Locate every blood parasite and identify its species.
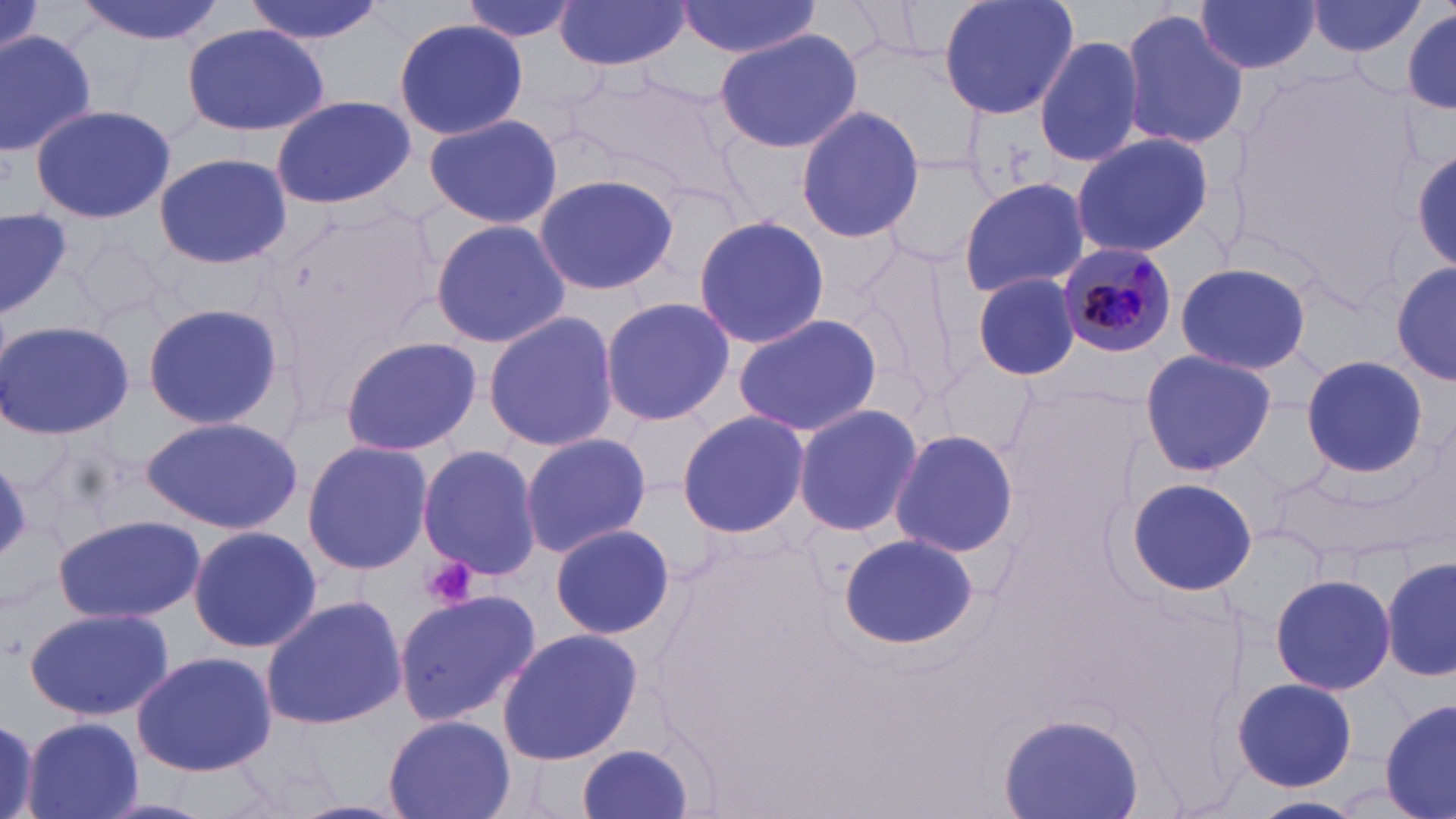
Approximate bounding boxes as (x1, y1, x2, y2) in pixels.
Plasmodium malariae-infected red blood cells: (1057, 242, 1182, 359).
No Plasmodium falciparum, Plasmodium ovale, Plasmodium vivax, Babesia divergens, or Trypanosoma brucei observed.

slide-level diagnosis = Plasmodium malariae
uninfected red blood cell locations = approximate bounding boxes as (x1, y1, x2, y2) in pixels: (70, 0, 230, 44), (243, 0, 382, 45), (465, 0, 578, 45), (939, 0, 1080, 123), (1194, 0, 1321, 75), (675, 1, 820, 58), (1306, 1, 1427, 58), (554, 2, 691, 70), (1398, 5, 1455, 117), (1121, 8, 1246, 152), (394, 16, 527, 140), (179, 23, 331, 137), (714, 28, 863, 155), (0, 29, 99, 157), (1035, 34, 1143, 170), (560, 70, 740, 191), (270, 95, 414, 209), (29, 102, 176, 226), (795, 103, 925, 246), (422, 112, 563, 231), (1068, 131, 1215, 259), (1409, 139, 1456, 279), (874, 147, 996, 267), (153, 152, 291, 270), (532, 170, 679, 298), (957, 178, 1091, 299), (261, 193, 445, 362), (0, 208, 72, 317), (693, 213, 830, 350), (429, 218, 570, 350), (67, 228, 171, 334), (846, 234, 971, 408), (1173, 260, 1314, 376), (1392, 262, 1453, 389), (970, 271, 1083, 381), (598, 296, 734, 428), (141, 301, 284, 431), (484, 311, 620, 452), (733, 312, 884, 437), (0, 318, 134, 442), (337, 336, 479, 456), (1139, 350, 1276, 477), (1301, 355, 1428, 477), (791, 402, 922, 538), (677, 407, 812, 540), (140, 414, 303, 533), (889, 426, 1020, 559), (519, 432, 653, 558), (301, 440, 435, 576), (417, 445, 544, 580), (1123, 476, 1258, 597), (55, 514, 201, 624), (550, 523, 675, 641), (184, 526, 324, 654), (835, 532, 982, 650), (1382, 556, 1456, 683), (1269, 571, 1396, 695), (397, 590, 541, 726), (259, 595, 409, 730), (25, 606, 174, 721), (496, 628, 643, 764), (133, 650, 278, 777), (1233, 678, 1357, 790), (1381, 698, 1456, 819), (1000, 711, 1144, 818), (0, 713, 39, 818), (381, 713, 516, 819), (22, 716, 144, 819), (573, 743, 699, 819), (1249, 794, 1367, 819)
image size = 1456×819 pixels
stain = May-Grünwald-Giemsa
magnification = 1000x
preparation = thin blood film
field of view = one of a larger specimen
platelet locations = approximate bounding boxes as (x1, y1, x2, y2) in pixels: (421, 554, 479, 609)
modality = optical microscopy